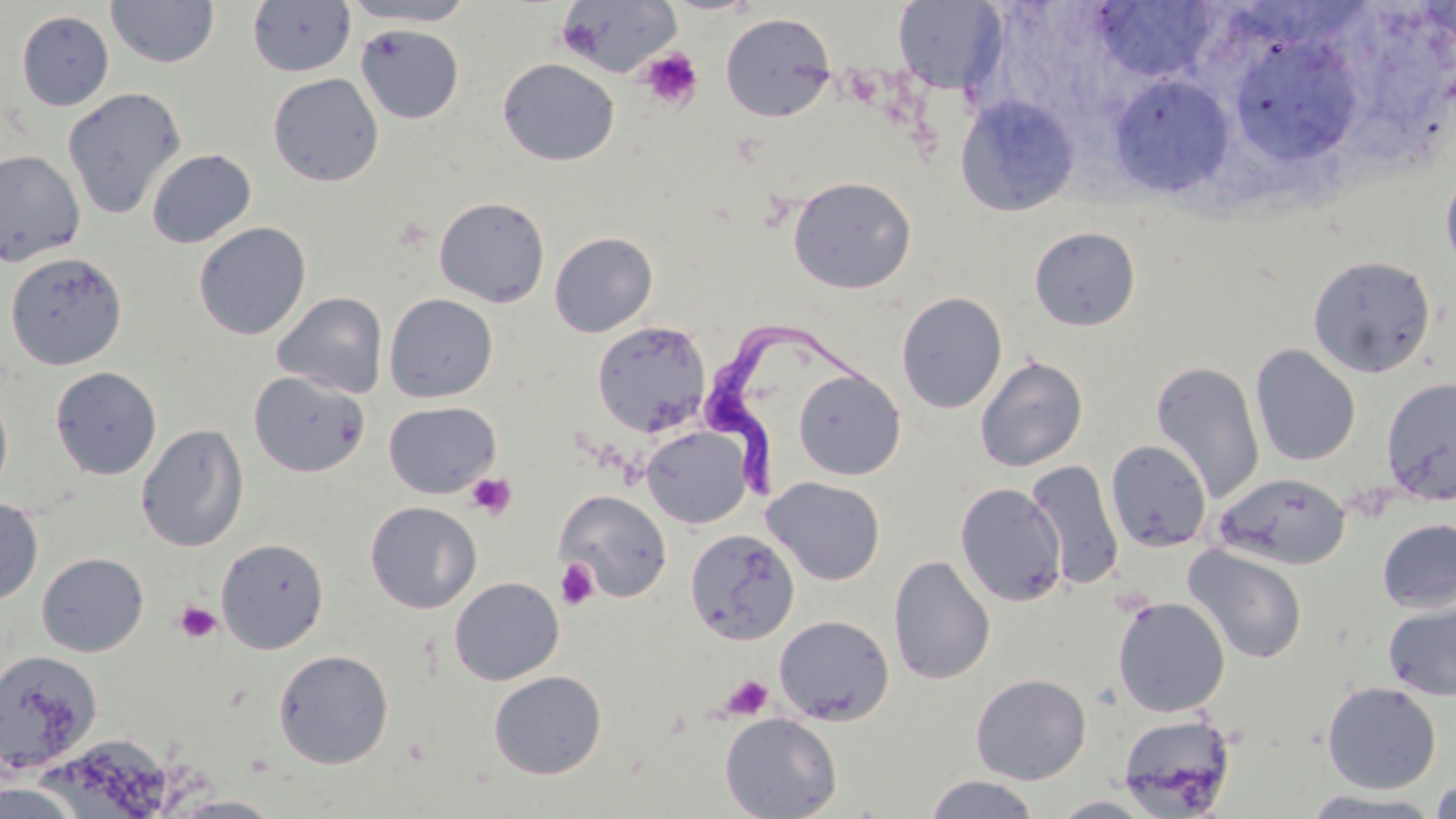
slide-level diagnosis = Trypanosoma brucei
modality = light microscopy
field of view = single
platelet locations = approximate bounding boxes as (x1, y1, x2, y2) in pixels: (640, 48, 703, 111), (466, 473, 517, 519), (556, 558, 599, 609), (174, 602, 222, 643), (721, 675, 773, 720)
preparation = thin blood film
image size = 1456×819 pixels
uninfected red blood cell locations = approximate bounding boxes as (x1, y1, x2, y2) in pixels: (106, 0, 219, 68), (343, 0, 476, 27), (555, 0, 682, 78), (247, 1, 356, 77), (892, 1, 1008, 94), (1098, 2, 1224, 82), (16, 10, 114, 111), (720, 12, 836, 122), (356, 23, 464, 124), (1240, 47, 1358, 156), (498, 58, 620, 166), (267, 72, 384, 187), (1110, 74, 1234, 197), (62, 87, 186, 220), (955, 94, 1080, 216), (146, 148, 256, 248), (0, 149, 85, 266), (1440, 164, 1456, 281), (788, 175, 917, 294), (433, 196, 551, 307), (193, 222, 311, 340), (1029, 227, 1141, 331), (549, 231, 658, 337), (4, 251, 128, 370), (1308, 255, 1436, 378), (272, 292, 388, 398), (896, 292, 1008, 413), (384, 293, 498, 402), (592, 321, 710, 437), (1250, 344, 1361, 466), (975, 355, 1088, 472), (1151, 360, 1265, 504), (50, 366, 161, 480), (793, 368, 906, 480), (248, 371, 370, 477), (1381, 376, 1456, 504), (0, 384, 14, 499), (383, 401, 501, 498), (136, 423, 249, 552), (642, 425, 753, 528), (1106, 440, 1212, 552), (1026, 460, 1125, 590), (1215, 472, 1351, 570), (762, 476, 885, 585), (955, 482, 1067, 606), (555, 490, 672, 602), (0, 497, 43, 606), (365, 500, 482, 613), (1377, 518, 1456, 614), (684, 528, 799, 646), (216, 538, 328, 653), (1183, 544, 1308, 665), (36, 552, 148, 657), (888, 555, 995, 685), (449, 576, 564, 685), (1112, 596, 1231, 717), (1383, 601, 1456, 701), (773, 614, 894, 725), (273, 649, 394, 768), (1, 650, 103, 773), (488, 670, 607, 779), (970, 673, 1091, 785), (1321, 681, 1441, 793), (720, 712, 842, 819), (1117, 713, 1236, 816), (48, 734, 176, 817), (924, 774, 1041, 819), (1431, 777, 1456, 819), (0, 780, 85, 819), (1299, 789, 1446, 817), (166, 795, 289, 818), (1050, 795, 1160, 818)
stain = May-Grünwald-Giemsa
Trypanosoma brucei locations = approximate bounding boxes as (x1, y1, x2, y2) in pixels: (708, 322, 870, 503)
magnification = 1000x